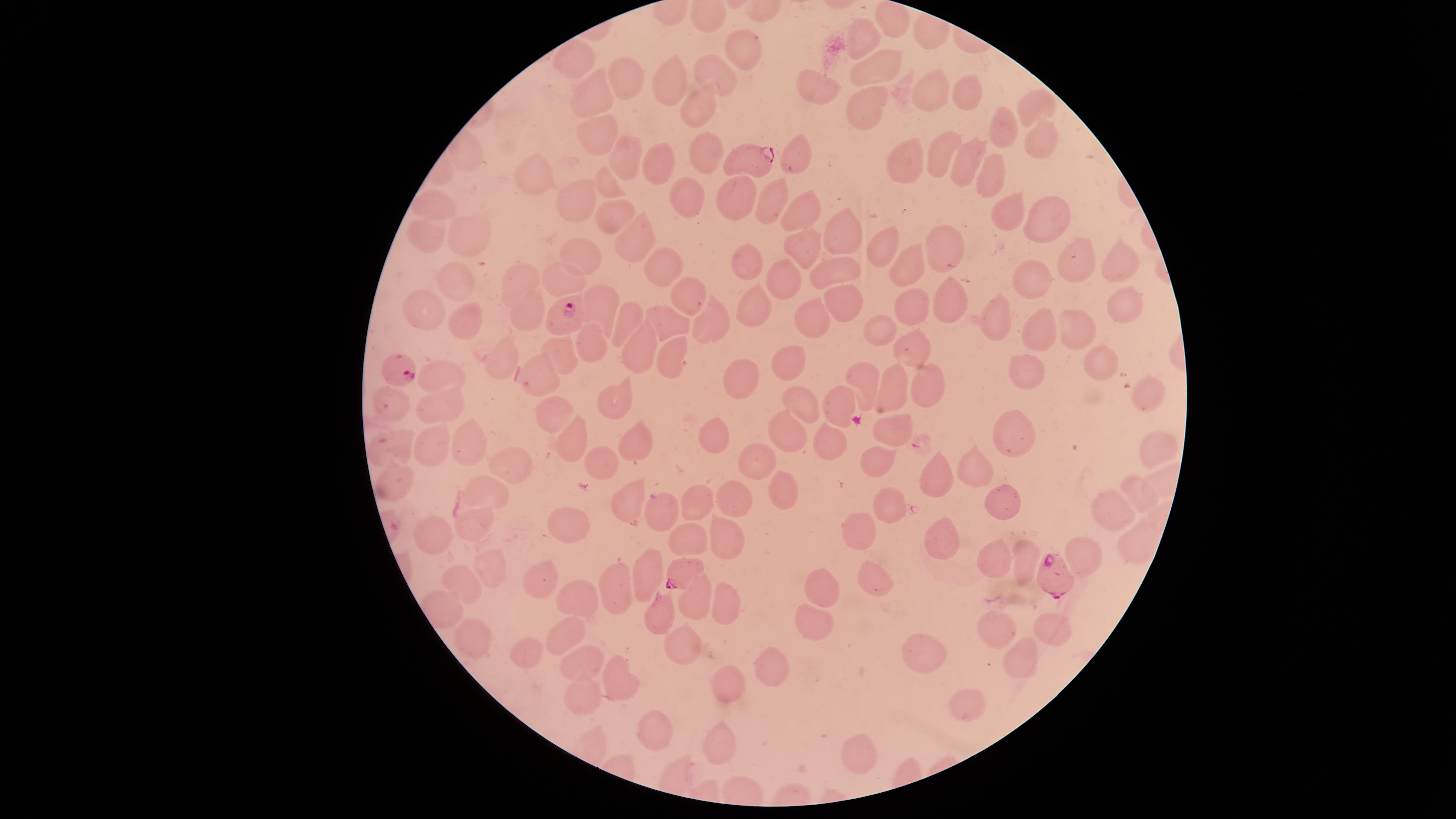
Approximate marker points as (x, y) in pixels.
Summary:
  - Uninfected RBCs: (863, 39), (746, 51), (579, 64), (866, 69), (717, 70), (626, 75), (674, 76), (820, 81), (932, 90), (964, 97), (590, 100), (857, 107), (1043, 107), (692, 108), (998, 125), (593, 133), (1032, 135), (937, 149), (701, 153), (798, 153), (623, 157), (903, 159), (966, 163), (657, 165), (985, 172), (539, 178), (609, 182), (688, 192), (736, 197), (575, 201), (436, 204), (766, 207), (799, 207), (1002, 210), (612, 212), (1039, 219), (840, 230), (427, 233), (462, 235), (629, 235), (805, 240), (948, 242), (885, 249), (657, 255), (579, 258), (1081, 258), (743, 262), (1124, 262), (910, 264), (836, 272), (1031, 273), (525, 277), (780, 280), (456, 282), (561, 283), (684, 289), (841, 296), (910, 298), (598, 300), (946, 300), (754, 305), (427, 309), (1133, 309), (528, 316), (813, 318), (994, 318), (672, 319), (470, 321), (627, 321), (717, 321), (881, 327), (1039, 330), (1078, 332), (587, 341), (640, 346), (909, 346), (561, 350), (672, 351), (503, 357), (1099, 357), (789, 360), (1022, 369), (440, 372), (739, 375), (865, 377), (541, 379), (928, 380), (891, 386), (1146, 388), (615, 396), (802, 405), (396, 406), (443, 406), (549, 410), (840, 413), (894, 431), (788, 432), (1017, 432), (717, 435), (572, 437), (635, 443), (829, 445), (397, 447), (479, 448), (1154, 448), (429, 449), (759, 462), (877, 464), (982, 465), (600, 466), (510, 472), (938, 476), (396, 480), (1134, 489), (782, 491), (483, 492), (732, 496), (1001, 500), (624, 502), (696, 502), (887, 508), (1113, 512), (654, 513), (566, 526), (864, 527), (475, 529), (685, 537), (724, 538), (432, 539), (946, 539), (1130, 541), (996, 561), (1025, 561), (646, 567), (870, 572), (487, 573), (543, 573), (464, 586), (828, 587), (619, 588), (695, 598), (580, 602), (725, 607), (660, 609), (815, 621), (1046, 624), (1006, 628), (564, 630), (473, 639), (683, 644), (533, 649), (914, 659), (1017, 659), (580, 668), (770, 668), (623, 677), (729, 683), (588, 695), (960, 713), (658, 726), (721, 736), (860, 742)
  - Parasitized RBCs: (742, 159), (563, 315), (398, 369), (680, 570), (1055, 576)
  - Visible region: circular
  - Presence: malaria parasites detected
  - Field of view: single
  - Capture: smartphone photograph through the microscope eyepiece
  - Stain: Giemsa
  - Preparation: thin blood smear
  - Image size: 1456×819 pixels
  - Species: Plasmodium falciparum